Identify the blood parasite species.
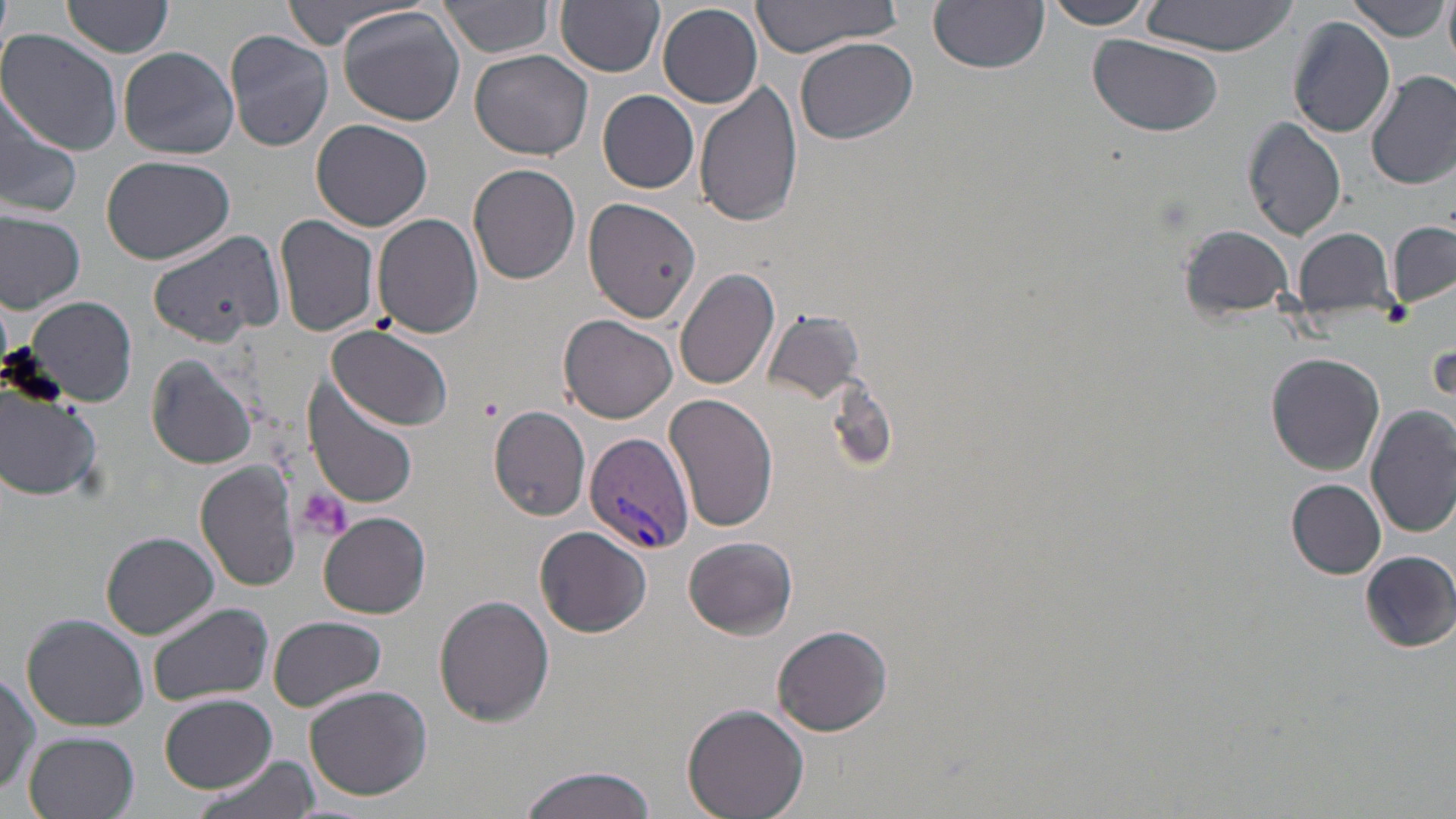
Plasmodium vivax.

platelet_locations: 'approximate bounding boxes as named x1/y1/x2/y2 corners in pixels: (x1=1377, y1=299, x2=1413, y2=328), (x1=291, y1=484, x2=352, y2=545)'
plasmodium_vivax_infected_red_blood_cell_locations: 'approximate bounding boxes as named x1/y1/x2/y2 corners in pixels: (x1=585, y1=432, x2=694, y2=554)'
field_of_view: single
magnification: 1000x
preparation: thin blood film
uninfected_red_blood_cell_locations: 'approximate bounding boxes as named x1/y1/x2/y2 corners in pixels: (x1=276, y1=0, x2=418, y2=51), (x1=438, y1=0, x2=557, y2=59), (x1=557, y1=0, x2=665, y2=75), (x1=749, y1=0, x2=906, y2=58), (x1=1040, y1=0, x2=1158, y2=29), (x1=1441, y1=0, x2=1456, y2=67), (x1=60, y1=1, x2=174, y2=61), (x1=930, y1=1, x2=1049, y2=73), (x1=1140, y1=1, x2=1295, y2=57), (x1=1349, y1=1, x2=1447, y2=43), (x1=658, y1=2, x2=764, y2=108), (x1=338, y1=8, x2=467, y2=126), (x1=1286, y1=16, x2=1395, y2=138), (x1=2, y1=30, x2=122, y2=154), (x1=225, y1=30, x2=334, y2=153), (x1=1087, y1=36, x2=1227, y2=139), (x1=795, y1=37, x2=919, y2=145), (x1=118, y1=46, x2=240, y2=161), (x1=470, y1=49, x2=593, y2=161), (x1=1365, y1=69, x2=1456, y2=190), (x1=695, y1=81, x2=804, y2=227), (x1=0, y1=90, x2=81, y2=220), (x1=598, y1=90, x2=699, y2=195), (x1=1242, y1=118, x2=1347, y2=241), (x1=312, y1=119, x2=435, y2=233), (x1=102, y1=155, x2=234, y2=265), (x1=467, y1=163, x2=581, y2=284), (x1=584, y1=198, x2=703, y2=322), (x1=0, y1=213, x2=86, y2=313), (x1=372, y1=213, x2=484, y2=339), (x1=275, y1=214, x2=382, y2=337), (x1=1389, y1=222, x2=1455, y2=308), (x1=1178, y1=224, x2=1298, y2=323), (x1=148, y1=227, x2=283, y2=346), (x1=1292, y1=227, x2=1401, y2=326), (x1=673, y1=267, x2=781, y2=391), (x1=22, y1=294, x2=138, y2=408), (x1=766, y1=309, x2=862, y2=402), (x1=558, y1=315, x2=677, y2=423), (x1=325, y1=325, x2=457, y2=434), (x1=1265, y1=352, x2=1385, y2=475), (x1=145, y1=355, x2=260, y2=469), (x1=1293, y1=371, x2=1446, y2=512), (x1=304, y1=375, x2=420, y2=507), (x1=1, y1=381, x2=104, y2=502), (x1=664, y1=391, x2=779, y2=533), (x1=488, y1=405, x2=592, y2=521), (x1=1367, y1=406, x2=1456, y2=539), (x1=196, y1=463, x2=302, y2=592), (x1=1287, y1=479, x2=1387, y2=578), (x1=320, y1=513, x2=431, y2=617), (x1=535, y1=525, x2=652, y2=637), (x1=101, y1=532, x2=219, y2=639), (x1=682, y1=535, x2=798, y2=640), (x1=1358, y1=548, x2=1454, y2=651), (x1=435, y1=596, x2=556, y2=725), (x1=148, y1=603, x2=273, y2=708), (x1=23, y1=615, x2=148, y2=731), (x1=267, y1=615, x2=388, y2=709), (x1=772, y1=623, x2=894, y2=737), (x1=1, y1=669, x2=39, y2=804), (x1=302, y1=684, x2=433, y2=802), (x1=158, y1=694, x2=277, y2=792), (x1=683, y1=702, x2=809, y2=818), (x1=24, y1=732, x2=140, y2=819), (x1=194, y1=755, x2=322, y2=819), (x1=516, y1=765, x2=659, y2=819)'
image_size: 1456×819 pixels
stain: May-Grünwald-Giemsa
modality: light microscopy